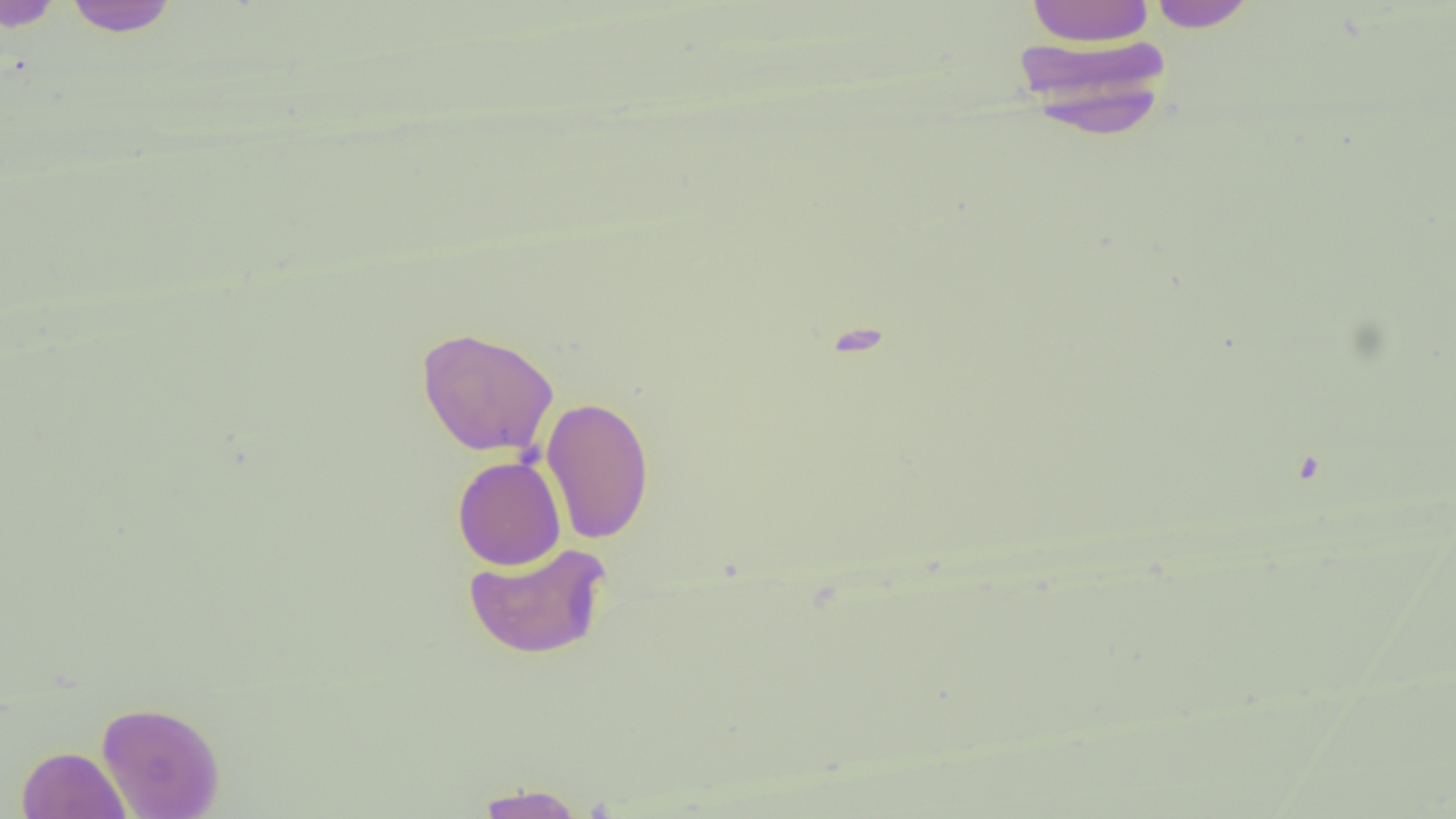
Approximate bounding boxes as [x1, y1, x2, y2] in pixels. Uninfected red blood cell locations: [62, 0, 181, 37], [1025, 0, 1155, 46], [0, 1, 68, 32], [1144, 1, 1259, 32], [1011, 35, 1173, 136], [417, 326, 559, 458], [540, 396, 655, 544], [452, 456, 566, 571], [462, 540, 612, 660], [96, 700, 225, 818], [16, 746, 132, 819], [473, 783, 587, 818]. Slide-level diagnosis: negative for blood parasites. Thin blood film. Image is 1456×819 pixels. Light microscopy. One field of a larger specimen. Captured at 1000x magnification.